Assess this cell for malaria.
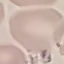
Uninfected.

stain: Giemsa
image_type: automatically extracted cell patch, resized to 64 × 64 pixels
preparation: thin blood film
capture: smartphone through the microscope eyepiece